Assess this cell for malaria.
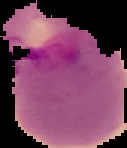
Parasitized.

Summary:
  - Preparation: thin blood film
  - Image size: 127×148 pixels
  - Image type: segmented cell region with the area outside set to black